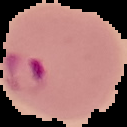

From a thin blood film. Segmented cell region on a black background. Image is 127×127 pixels. Malaria status: parasitized.